Name the cell type shown.
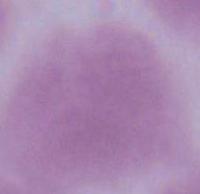
An erythrocyte.

1000x magnification. Photomicrograph.